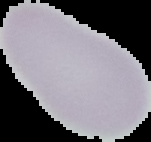

Summary:
  - Image type: segmented cell region on a black background
  - Preparation: thin blood film
  - Image size: 151×142 pixels
  - Malaria status: uninfected